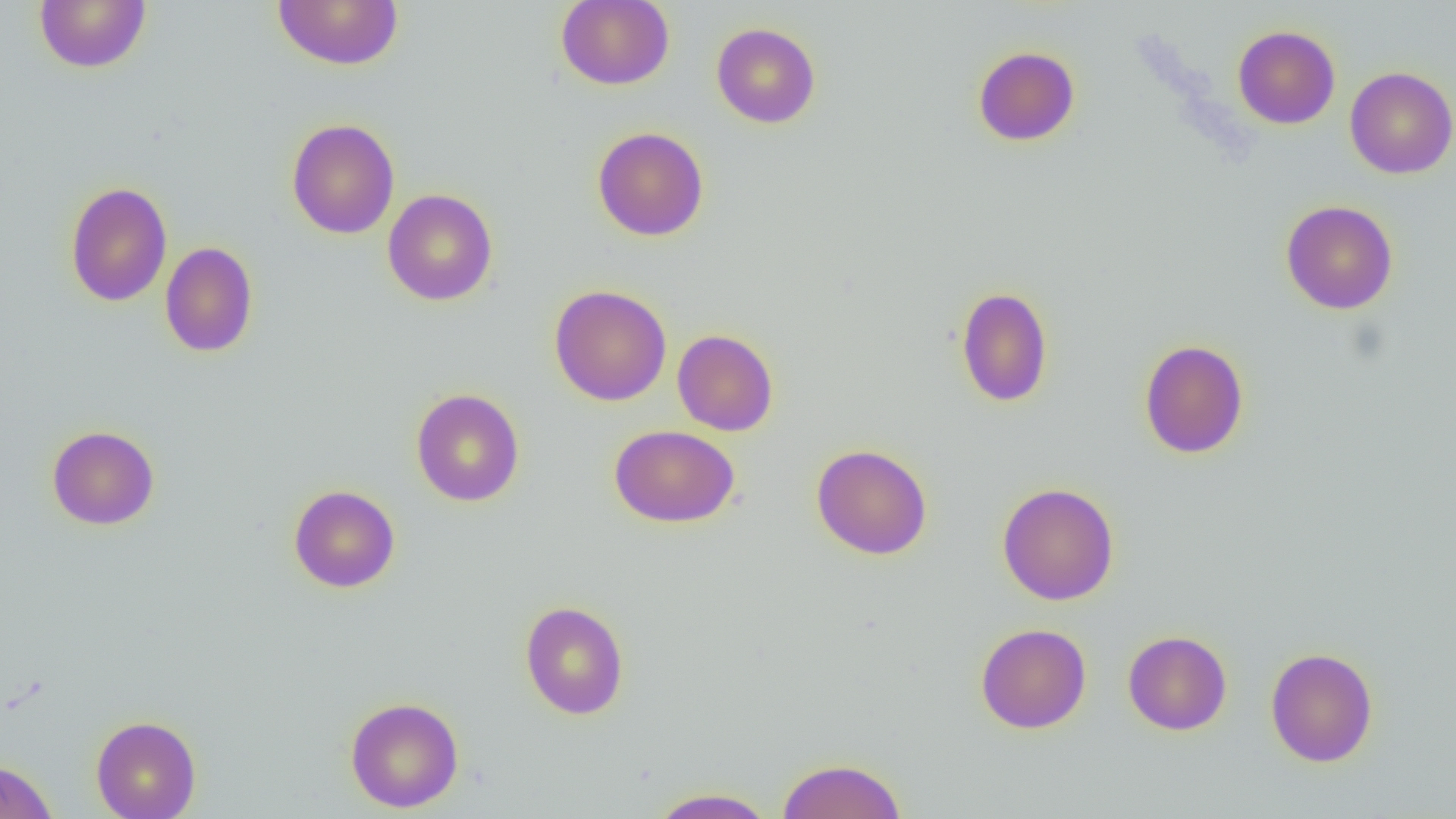
Approximate bounding boxes as (x1, y1, x2, y2) in pixels. Uninfected red blood cell locations: (34, 0, 152, 73), (272, 0, 404, 70), (555, 0, 675, 91), (711, 22, 821, 129), (1232, 25, 1341, 129), (973, 46, 1080, 146), (1344, 66, 1456, 179), (286, 118, 400, 239), (592, 126, 709, 241), (64, 181, 173, 307), (382, 188, 498, 306), (1280, 199, 1398, 314), (160, 242, 259, 358), (549, 285, 672, 406), (955, 286, 1054, 408), (672, 329, 779, 436), (1139, 339, 1249, 459), (410, 388, 525, 507), (47, 425, 160, 530), (609, 425, 740, 528), (811, 443, 933, 560), (996, 481, 1120, 606), (288, 484, 401, 593), (519, 600, 630, 720), (975, 623, 1092, 734), (1123, 630, 1232, 736), (1265, 647, 1378, 767), (345, 696, 464, 812), (90, 714, 201, 819), (776, 757, 907, 818), (0, 760, 57, 819), (647, 787, 778, 818). Slide-level diagnosis: no evidence of blood parasites. One field of a larger specimen. Captured at 1000x magnification. Thin blood smear. Optical microscopy. Image is 1456×819 pixels.